Assess the morphology of the red blood cells.
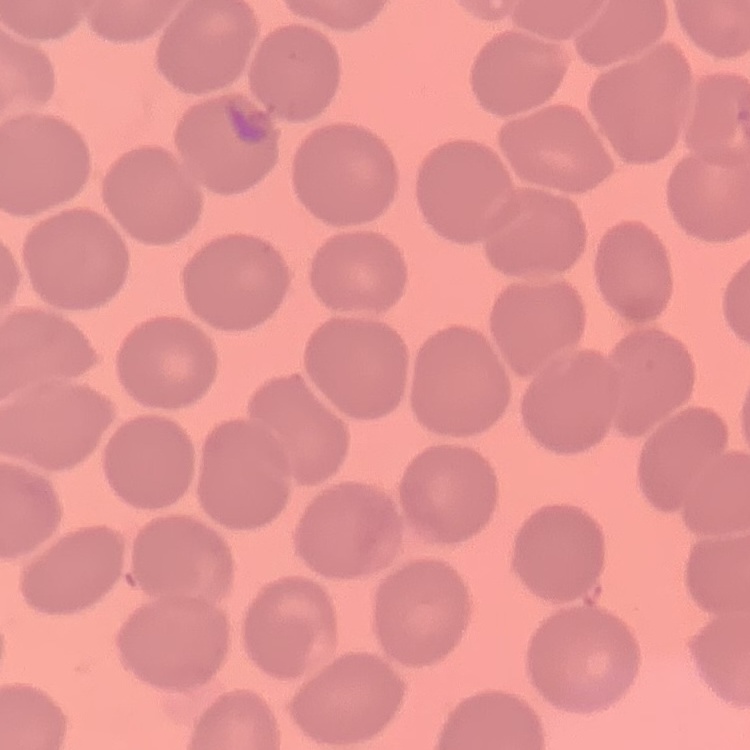

No rouleaux formation.

Summary:
  - Stain: Field's or Giemsa
  - Image type: square crop of a larger photomicrograph
  - Preparation: thin blood film